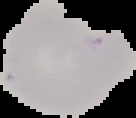
image type = cell region segmented out of the field of view; surrounding area masked to black
preparation = thin blood smear
image size = 136×118 pixels
result = no Plasmodium parasites detected